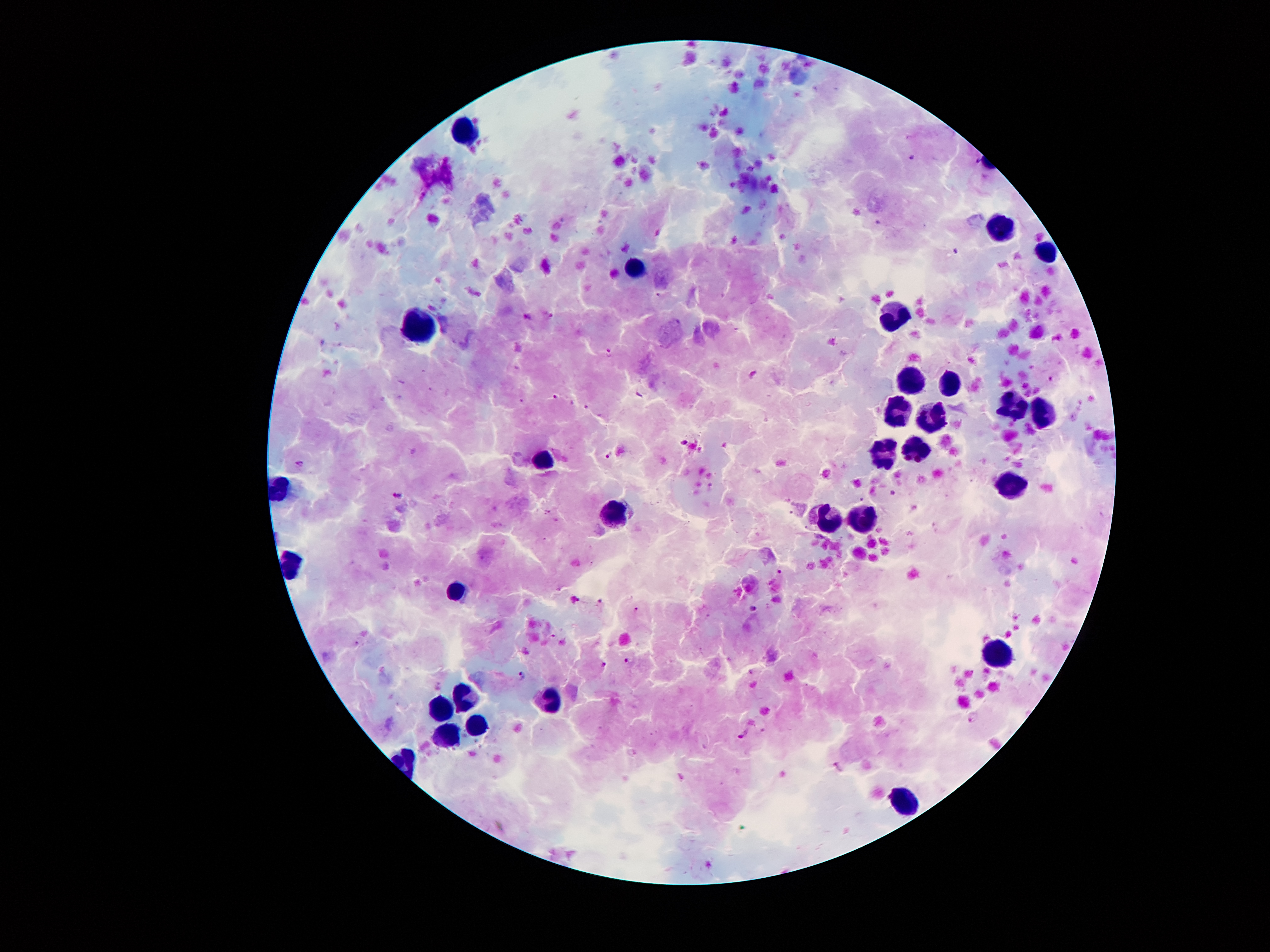 Approximate centers as [x, y] in pixels. Leukocyte locations: [467, 130], [996, 222], [1049, 251], [636, 263], [892, 316], [413, 336], [907, 378], [949, 385], [1013, 409], [894, 412], [1044, 416], [931, 422], [915, 450], [879, 454], [538, 460], [1011, 489], [620, 514], [832, 517], [864, 524], [461, 590], [996, 658], [460, 697], [545, 702], [445, 709], [477, 725], [446, 733], [904, 804]. Plasmodium parasite locations: [912, 158], [955, 251], [528, 316], [548, 316], [610, 353], [756, 374], [557, 396], [684, 442], [610, 455], [300, 464], [397, 495], [778, 572], [599, 602], [637, 608], [753, 609], [628, 660], [606, 665], [522, 676], [973, 717], [744, 734], [837, 767]. Thick blood smear. Patient malaria status: infected with Plasmodium falciparum. 100x magnification. Giemsa stain. Image is 1270×952 pixels. Single field of view. Photographed through the microscope eyepiece with a smartphone camera.